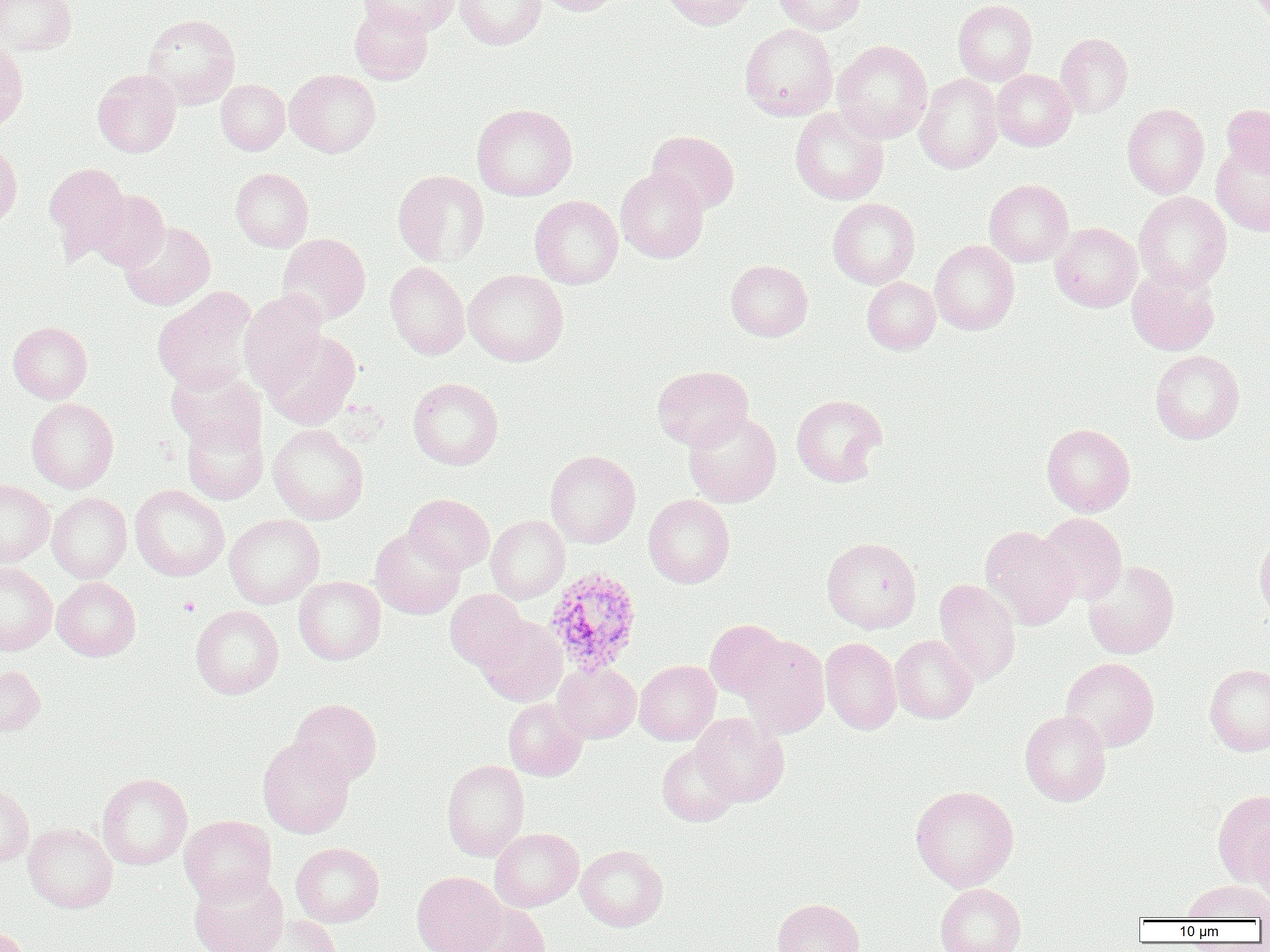
Summary:
  - Coordinate format: approximate bounding boxes as named x1/y1/x2/y2 corners in pixels
  - Plasmodium ovale-infected red blood cell locations: (x1=543, y1=567, x2=643, y2=676)
  - Platelet locations: (x1=179, y1=597, x2=201, y2=617)
  - Uninfected red blood cell locations: (x1=0, y1=0, x2=77, y2=55), (x1=358, y1=0, x2=458, y2=36), (x1=455, y1=0, x2=546, y2=48), (x1=535, y1=0, x2=621, y2=16), (x1=664, y1=0, x2=756, y2=29), (x1=774, y1=0, x2=865, y2=34), (x1=953, y1=0, x2=1037, y2=85), (x1=349, y1=3, x2=434, y2=84), (x1=143, y1=14, x2=240, y2=108), (x1=740, y1=23, x2=838, y2=120), (x1=1055, y1=32, x2=1133, y2=117), (x1=832, y1=39, x2=932, y2=143), (x1=0, y1=41, x2=28, y2=133), (x1=92, y1=69, x2=181, y2=157), (x1=285, y1=69, x2=380, y2=157), (x1=992, y1=69, x2=1076, y2=151), (x1=915, y1=73, x2=1003, y2=174), (x1=216, y1=79, x2=290, y2=155), (x1=472, y1=103, x2=577, y2=201), (x1=1122, y1=103, x2=1209, y2=198), (x1=1222, y1=104, x2=1270, y2=177), (x1=790, y1=107, x2=888, y2=205), (x1=648, y1=130, x2=740, y2=213), (x1=0, y1=141, x2=22, y2=230), (x1=1212, y1=143, x2=1270, y2=236), (x1=44, y1=162, x2=131, y2=261), (x1=230, y1=168, x2=314, y2=252), (x1=616, y1=168, x2=708, y2=263), (x1=393, y1=169, x2=489, y2=267), (x1=984, y1=179, x2=1073, y2=267), (x1=87, y1=189, x2=169, y2=271), (x1=1134, y1=191, x2=1232, y2=292), (x1=530, y1=195, x2=623, y2=289), (x1=828, y1=198, x2=920, y2=289), (x1=120, y1=221, x2=216, y2=310), (x1=1050, y1=222, x2=1142, y2=312), (x1=277, y1=233, x2=371, y2=324), (x1=930, y1=240, x2=1019, y2=334), (x1=726, y1=259, x2=813, y2=341), (x1=385, y1=261, x2=469, y2=360), (x1=1127, y1=266, x2=1220, y2=356), (x1=464, y1=269, x2=568, y2=366), (x1=862, y1=277, x2=940, y2=354), (x1=153, y1=287, x2=258, y2=394), (x1=239, y1=289, x2=328, y2=394), (x1=8, y1=321, x2=92, y2=403), (x1=262, y1=329, x2=361, y2=429), (x1=1150, y1=350, x2=1244, y2=444), (x1=652, y1=365, x2=753, y2=450), (x1=166, y1=367, x2=266, y2=452), (x1=408, y1=377, x2=503, y2=470), (x1=791, y1=394, x2=887, y2=486), (x1=27, y1=398, x2=119, y2=492), (x1=684, y1=411, x2=781, y2=507), (x1=181, y1=413, x2=268, y2=505), (x1=1042, y1=423, x2=1136, y2=516), (x1=267, y1=424, x2=368, y2=524), (x1=545, y1=450, x2=641, y2=548), (x1=0, y1=479, x2=54, y2=567), (x1=130, y1=485, x2=230, y2=581), (x1=46, y1=492, x2=132, y2=582), (x1=404, y1=493, x2=494, y2=573), (x1=644, y1=494, x2=735, y2=588), (x1=1037, y1=512, x2=1127, y2=603), (x1=224, y1=514, x2=324, y2=608), (x1=486, y1=515, x2=569, y2=603), (x1=980, y1=525, x2=1079, y2=629), (x1=370, y1=527, x2=465, y2=619), (x1=1255, y1=534, x2=1270, y2=625), (x1=822, y1=537, x2=921, y2=633), (x1=1083, y1=559, x2=1179, y2=659), (x1=0, y1=562, x2=57, y2=655), (x1=294, y1=576, x2=385, y2=664), (x1=53, y1=577, x2=141, y2=660), (x1=933, y1=579, x2=1021, y2=685), (x1=445, y1=589, x2=529, y2=671), (x1=190, y1=605, x2=283, y2=698), (x1=475, y1=615, x2=567, y2=706), (x1=704, y1=619, x2=788, y2=702), (x1=739, y1=635, x2=830, y2=737), (x1=890, y1=635, x2=977, y2=723), (x1=820, y1=637, x2=901, y2=734), (x1=1060, y1=657, x2=1159, y2=752), (x1=634, y1=660, x2=720, y2=745), (x1=552, y1=662, x2=640, y2=743), (x1=0, y1=664, x2=45, y2=736), (x1=1204, y1=664, x2=1270, y2=755), (x1=290, y1=698, x2=382, y2=786), (x1=503, y1=698, x2=588, y2=780), (x1=1020, y1=711, x2=1111, y2=806), (x1=691, y1=713, x2=789, y2=806), (x1=258, y1=736, x2=354, y2=838), (x1=656, y1=742, x2=741, y2=827), (x1=441, y1=759, x2=529, y2=861), (x1=97, y1=773, x2=192, y2=869), (x1=0, y1=785, x2=34, y2=867), (x1=910, y1=785, x2=1019, y2=891), (x1=1213, y1=789, x2=1270, y2=886), (x1=179, y1=815, x2=277, y2=905), (x1=1252, y1=820, x2=1270, y2=903), (x1=23, y1=822, x2=117, y2=913), (x1=490, y1=828, x2=584, y2=911), (x1=291, y1=842, x2=384, y2=927), (x1=575, y1=845, x2=668, y2=931), (x1=189, y1=870, x2=288, y2=952), (x1=412, y1=871, x2=506, y2=952), (x1=1184, y1=880, x2=1269, y2=921), (x1=935, y1=883, x2=1026, y2=952), (x1=772, y1=897, x2=864, y2=952), (x1=457, y1=901, x2=550, y2=951), (x1=250, y1=915, x2=342, y2=952), (x1=0, y1=926, x2=32, y2=952)
  - Slide-level diagnosis: Plasmodium ovale
  - Preparation: thin blood film
  - Modality: optical microscopy
  - Field of view: single
  - Image size: 1270×952 pixels
  - Magnification: 1000x